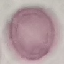
malaria_status: uninfected
image_type: automatically extracted cell patch, resized to 64 × 64 pixels
capture: smartphone through the microscope eyepiece
stain: Giemsa
preparation: thin blood film